Describe the morphology of the erythrocytes.
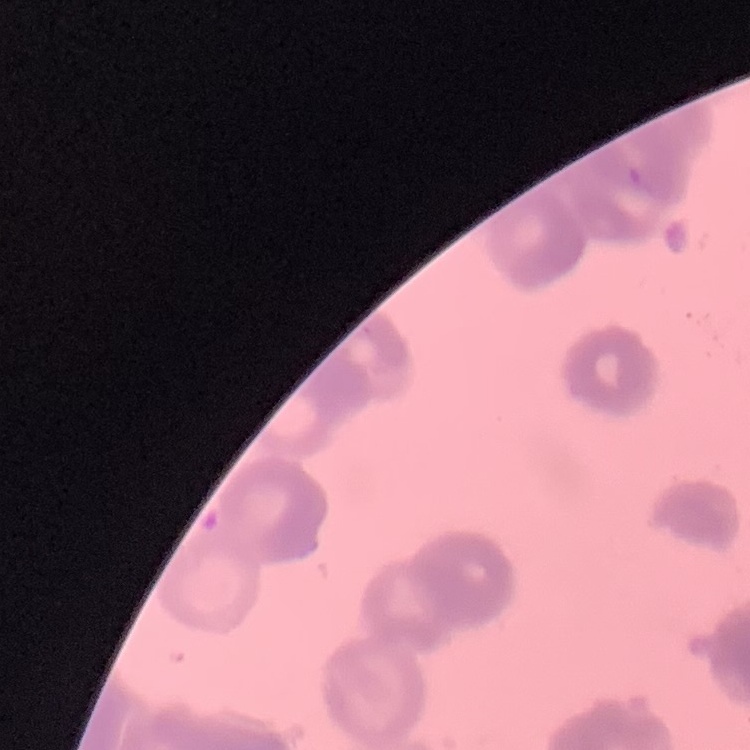

They show rouleaux formation.

Field's or Giemsa stain. Square crop of a larger photomicrograph. Thin blood film.